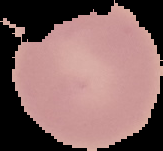
Summary:
  - Image size: 163×151 pixels
  - Image type: cell region segmented out of the field of view; surrounding area masked to black
  - Preparation: thin blood smear
  - Result: no malaria parasites detected